Assess this cell for malaria.
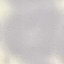

Uninfected.

Summary:
  - Preparation: thin smear
  - Stain: Giemsa
  - Image type: automatically extracted cell patch, resized to 64 × 64 pixels
  - Capture: smartphone camera at the microscope eyepiece